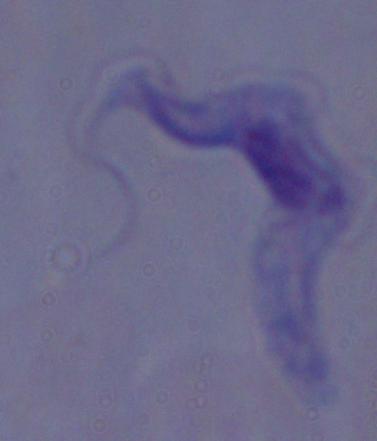

Summary:
  - Magnification: 1000x
  - Identification: trypanosome
  - Modality: micrograph